Classify this cell by malaria status.
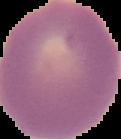

It is uninfected.

The area outside the segmented cell region is set to black. Image is 121×139 pixels. From a thin blood smear.